Assess this cell for malaria.
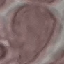
It is uninfected.

stain = Giemsa
image type = cell patch, automatically extracted from a larger field of view and resized to 64 × 64 pixels
preparation = thin blood film
capture = smartphone through the microscope eyepiece